Comment on the morphology of the erythrocytes.
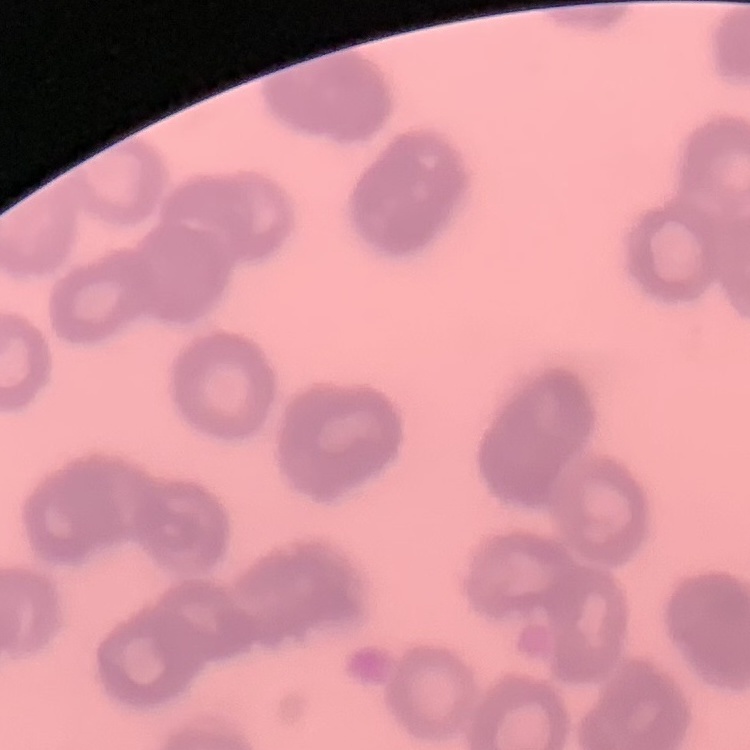
They show rouleaux formation.

Summary:
  - Image type: square crop of a larger photomicrograph
  - Preparation: thin blood film
  - Stain: Field's or Giemsa